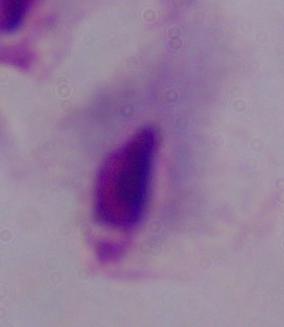 1000x magnification. A trichomonad is shown. Photomicrograph.